Assess the morphology of the red blood cells.
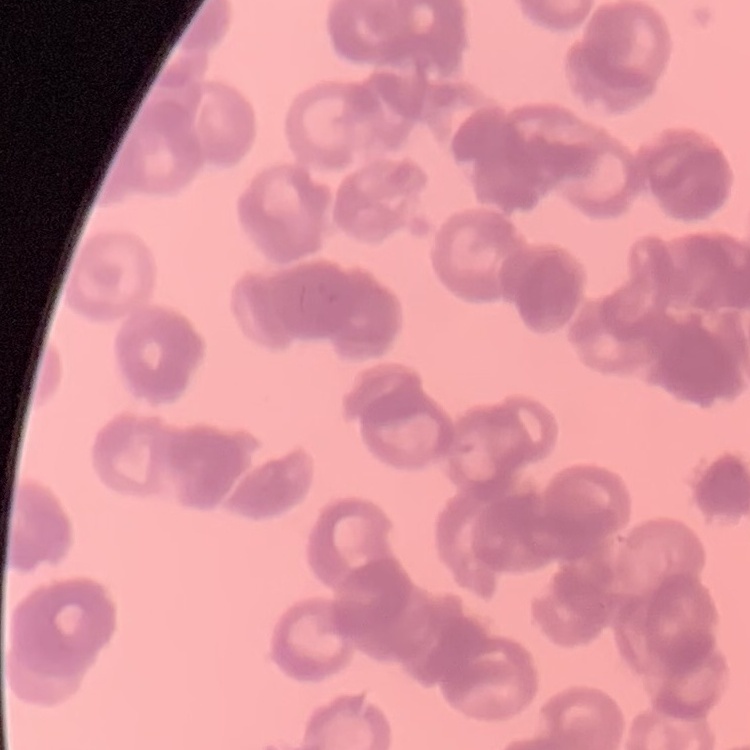
Rouleaux formation.

preparation: thin blood film
image_type: one tile cut from a larger photomicrograph
stain: Field's or Giemsa